State which parasite is depicted.
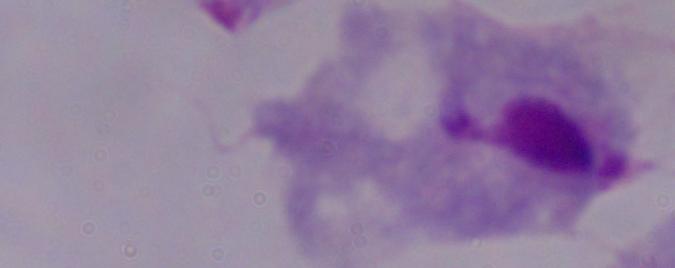
A trichomonad.

magnification = 1000x
modality = photomicrograph